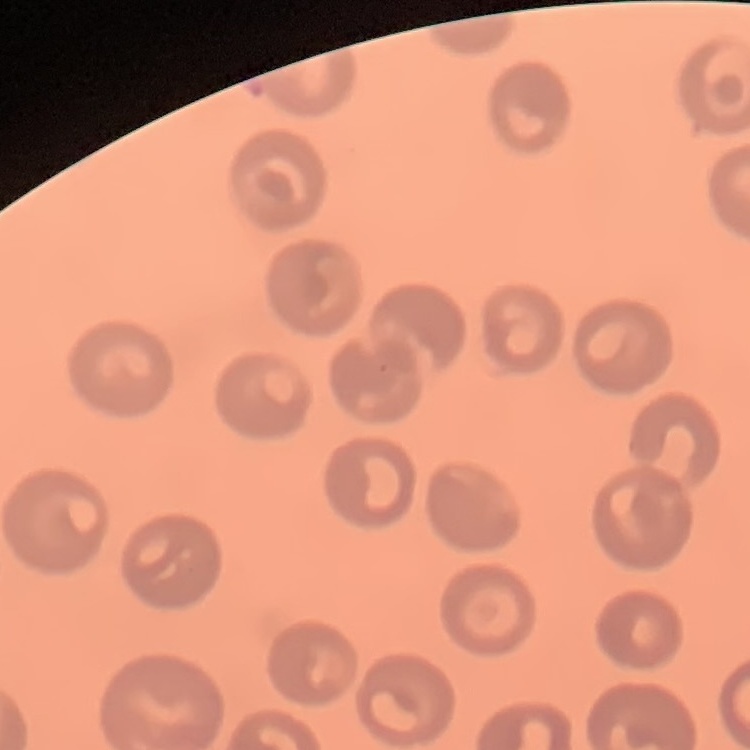
Summary:
  - Red blood cell morphology: no rouleaux formation
  - Image type: one tile cut from a larger photomicrograph
  - Preparation: thin blood film
  - Stain: Field's or Giemsa